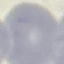 Result: negative for malaria parasites. Giemsa-stained preparation. Thin blood smear. Cell patch, automatically extracted from a larger field of view and resized to 64 × 64 pixels. Acquired by smartphone through the microscope eyepiece.